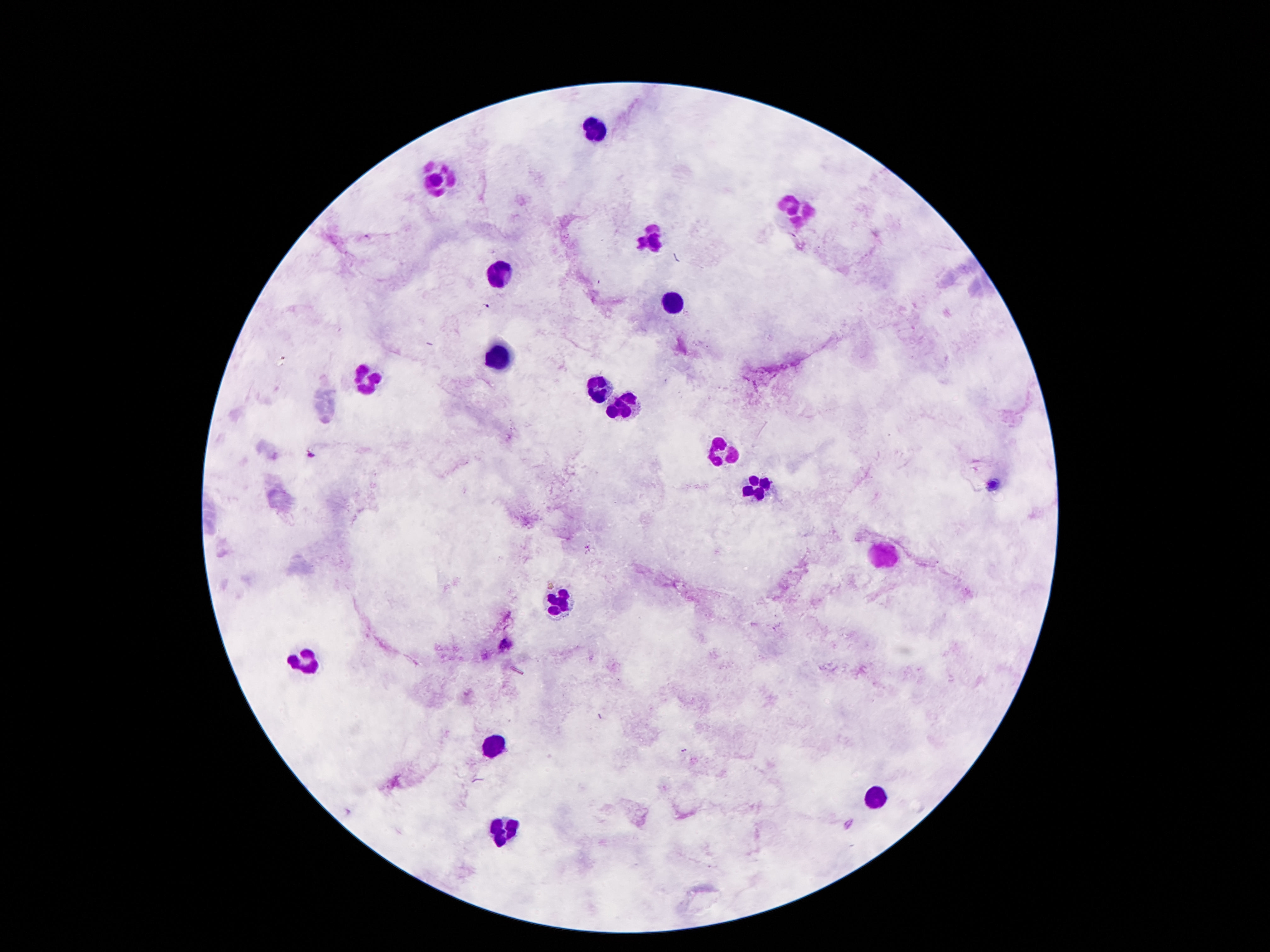

Approximate centers as [x, y] in pixels. Leukocyte locations: [595, 129], [437, 178], [800, 212], [648, 238], [501, 275], [673, 302], [497, 356], [370, 380], [599, 390], [622, 404], [720, 453], [753, 488], [880, 554], [556, 602], [302, 660], [497, 746], [876, 798], [505, 831]. Photographed through the microscope eyepiece with a smartphone camera. 100x magnification. Image is 1270×952 pixels. Thick blood film. Patient malaria status: not infected. One field from this slide. Giemsa stain.